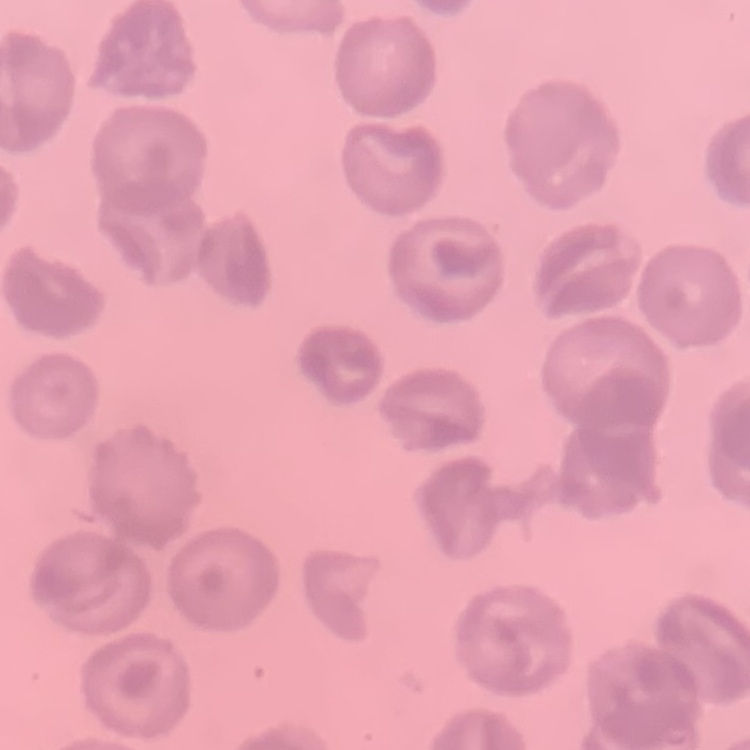
erythrocyte morphology = no rouleaux formation
image type = one tile cut from a larger photomicrograph
stain = Field's or Giemsa
preparation = thin blood smear